Comment on the morphology of the red blood cells.
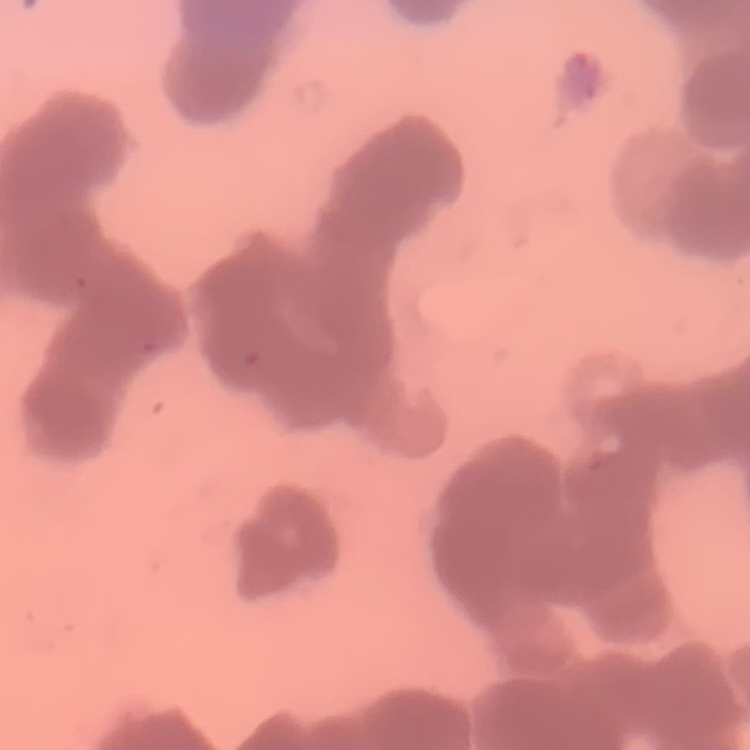
Rouleaux formation.

stain = Field's or Giemsa
preparation = thin peripheral smear
image type = one tile cut from a larger photomicrograph